Assess this cell for malaria.
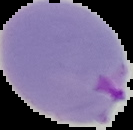
Parasitized.

Summary:
  - Image type: segmented cell region on a black background
  - Image size: 133×130 pixels
  - Preparation: thin blood smear